Assess this cell for malaria.
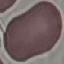
It is uninfected.

Cell patch, automatically extracted from a larger field of view and resized to 64 × 64 pixels. Giemsa stain. Thin blood film. Photographed with a smartphone camera at the microscope eyepiece.